Report the malaria status.
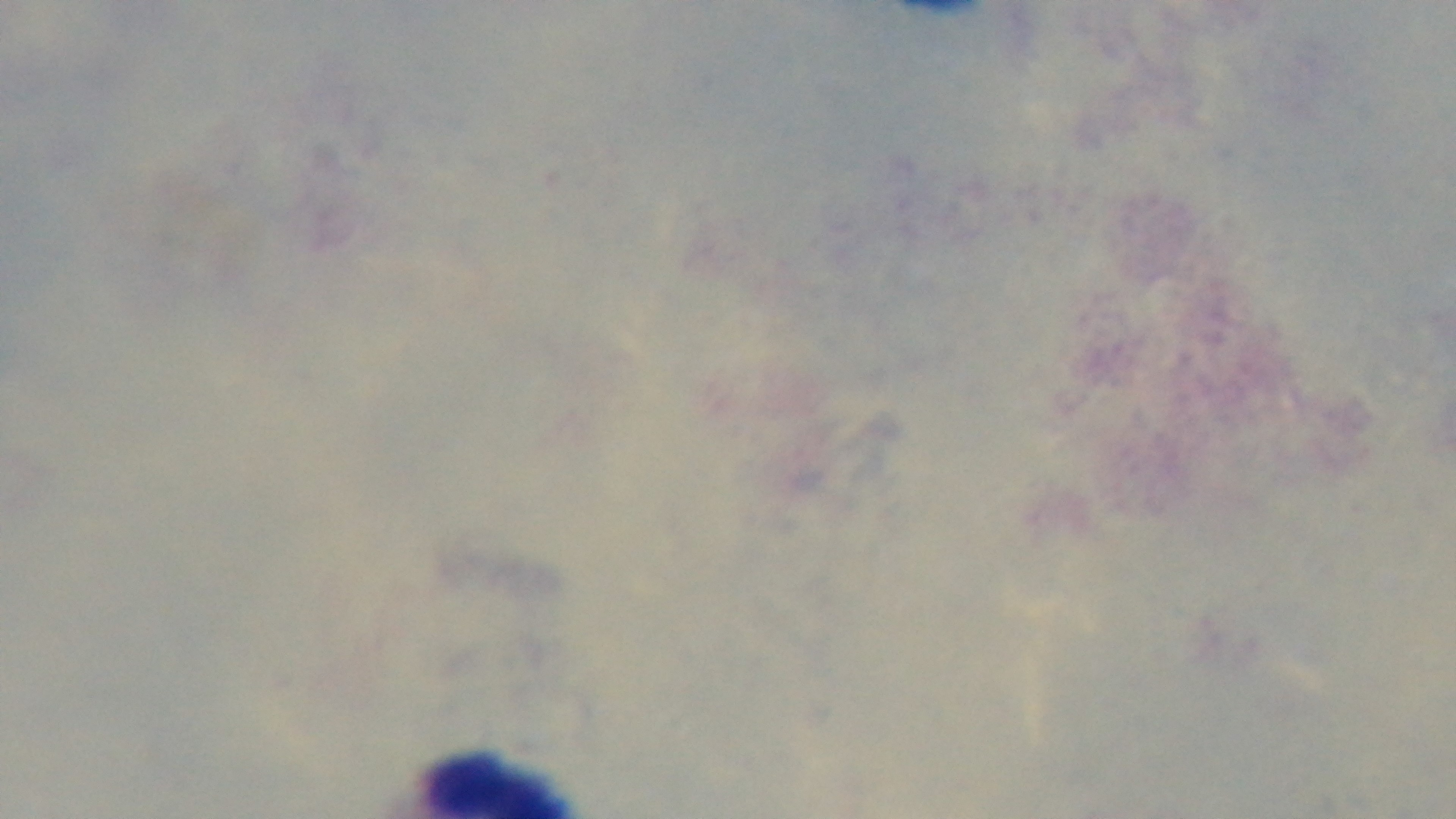
Uninfected.

Preparation: thick smear. Mounted 4K digital camera. 100x oil-immersion objective. One field from the slide. Light microscopy. Giemsa-stained.